Name the parasite shown.
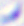

Toxoplasma gondii.

modality = photomicrograph
magnification = 400x